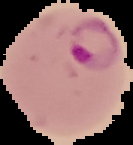

From a thin blood film. Image is 133×145 pixels. The area outside the segmented cell region is set to black. Malaria status: parasitized.